Name the parasite shown.
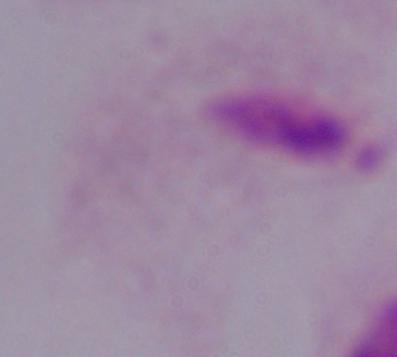

This is a trichomonad.

Photomicrograph. 1000x magnification.